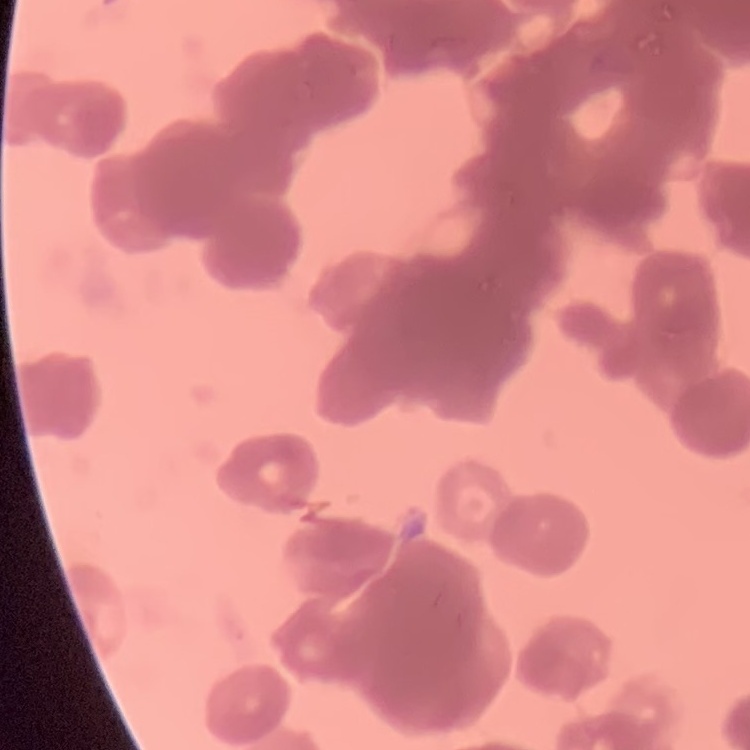
Summary:
  - Erythrocyte morphology: rouleaux formation
  - Image type: one tile cut from a larger photomicrograph
  - Preparation: thin peripheral smear
  - Stain: Field's or Giemsa